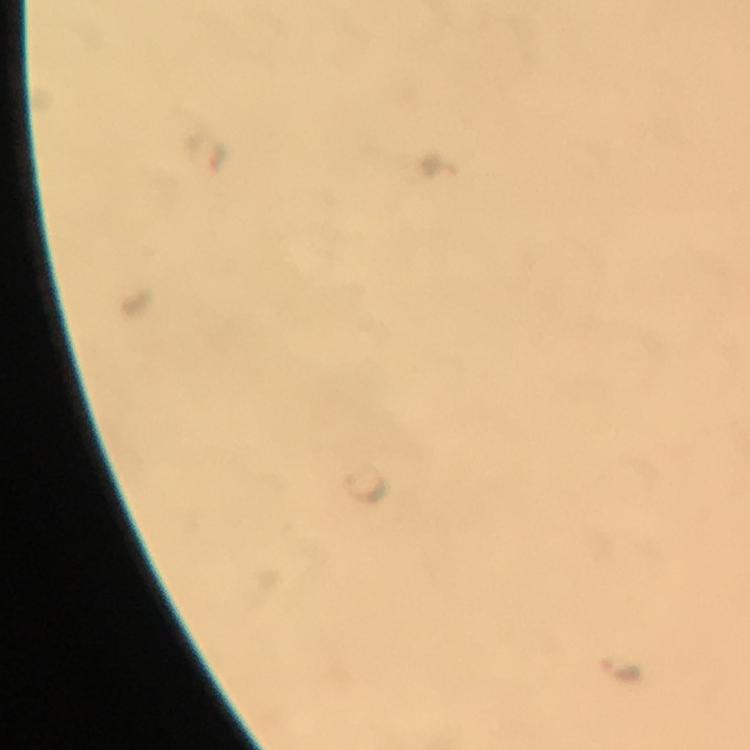
Approximate centers as (x, y) in pixels.
Summary:
  - Malaria parasite locations: (620, 663)
  - Stain: Giemsa
  - Magnification: 100x
  - Context: from a diagnostic examination for malaria
  - Immersion oil: applied
  - Image size: 750×750 pixels
  - Cropped from: a single field of view
  - Capture: smartphone camera through the microscope
  - Preparation: thick smear